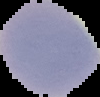 The area outside the segmented cell region is set to black. Image is 100×97 pixels. Result: no malaria parasites detected. From a thin blood smear.